Outline each blood parasite and name the species.
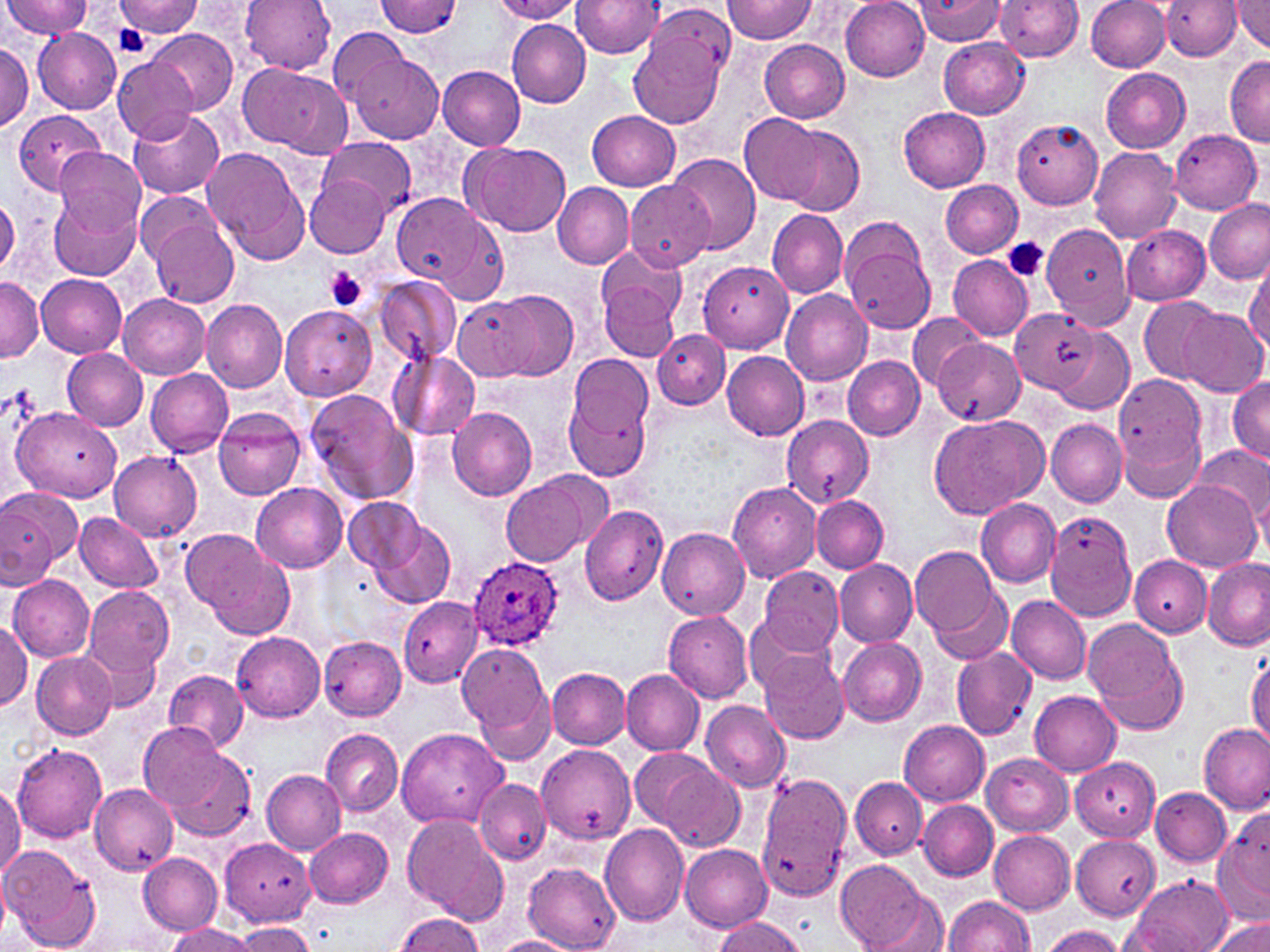

Approximate bounding boxes as (x1,y1)-(x2,y2) corner pairs in pixels.
Plasmodium ovale-infected red blood cells: (469,557)-(563,651).
No Plasmodium falciparum, Plasmodium malariae, Plasmodium vivax, Babesia divergens, or Trypanosoma brucei observed.

slide-level diagnosis = Plasmodium ovale
uninfected red blood cell locations = approximate bounding boxes as (x1,y1)-(x2,y2) corner pairs in pixels: (241,0)-(338,73), (377,0)-(463,37), (720,0)-(816,44), (840,0)-(931,81), (913,0)-(1006,45), (994,0)-(1084,61), (1086,0)-(1170,72), (1162,0)-(1244,61), (1231,0)-(1270,53), (0,1)-(89,40), (113,1)-(203,37), (489,1)-(580,23), (571,1)-(665,59), (637,2)-(734,80), (507,19)-(591,108), (32,26)-(121,114), (327,27)-(414,110), (630,27)-(725,131), (147,29)-(237,115), (939,38)-(1029,118), (759,40)-(849,124), (0,43)-(32,131), (350,52)-(441,143), (113,55)-(196,143), (1224,55)-(1270,146), (238,63)-(347,153), (437,65)-(526,150), (1100,68)-(1191,152), (898,106)-(991,192), (12,110)-(106,194), (128,110)-(225,199), (587,110)-(680,191), (740,114)-(824,205), (1011,119)-(1103,209), (776,123)-(864,215), (1169,127)-(1262,214), (321,136)-(413,214), (463,141)-(571,234), (1089,146)-(1180,244), (55,147)-(146,236), (201,148)-(305,253), (669,152)-(760,254), (305,175)-(390,257), (625,180)-(716,273), (939,180)-(1021,257), (553,183)-(632,269), (136,190)-(225,270), (393,193)-(484,285), (49,195)-(141,280), (0,199)-(19,278), (1203,199)-(1270,284), (767,209)-(847,299), (149,216)-(239,308), (839,217)-(938,335), (435,218)-(508,306), (1041,222)-(1137,327), (1122,225)-(1211,305), (948,255)-(1033,340), (1245,258)-(1270,356), (698,261)-(793,353), (599,267)-(684,364), (36,275)-(126,358), (374,275)-(462,365), (0,279)-(42,363), (493,289)-(577,381), (781,290)-(872,386), (119,295)-(210,379), (1138,296)-(1220,384), (201,297)-(286,392), (456,297)-(537,380), (279,304)-(376,402), (1176,307)-(1265,396), (1010,308)-(1099,394), (907,313)-(985,390), (1052,328)-(1133,414), (653,330)-(731,409), (932,339)-(1026,426), (63,349)-(148,429), (390,350)-(480,443), (721,350)-(809,439), (843,356)-(924,440), (564,361)-(656,482), (146,368)-(234,458), (1112,372)-(1209,478), (1227,377)-(1270,463), (305,388)-(416,504), (11,405)-(122,502), (446,406)-(537,501), (214,409)-(306,501), (783,410)-(879,507), (933,413)-(1048,517), (1047,420)-(1127,508), (1121,425)-(1203,503), (1195,444)-(1270,522), (109,451)-(203,543), (500,476)-(590,567), (1163,479)-(1260,572), (726,481)-(821,584), (1253,481)-(1269,560), (250,483)-(348,573), (0,485)-(82,581), (344,495)-(427,576), (812,495)-(889,572), (976,498)-(1061,587), (579,505)-(668,605), (75,510)-(163,592), (1042,510)-(1140,620), (370,521)-(457,609), (657,528)-(749,620), (188,535)-(295,637), (911,548)-(1000,637), (1129,554)-(1211,638), (1201,558)-(1270,651), (835,559)-(917,647), (758,566)-(845,654), (8,573)-(95,660), (84,587)-(175,677), (933,588)-(1013,663), (1008,594)-(1091,684), (399,596)-(482,687), (663,610)-(754,703), (744,615)-(831,693), (1083,619)-(1187,734), (0,620)-(32,711), (232,632)-(326,720), (837,635)-(926,726), (319,636)-(405,720), (88,637)-(163,714), (459,641)-(553,752), (951,647)-(1037,738), (31,649)-(116,739), (761,651)-(848,743), (1246,655)-(1270,749), (621,668)-(704,754), (547,669)-(631,749), (163,670)-(247,749), (1030,690)-(1121,776), (701,700)-(790,792), (898,719)-(990,805), (138,723)-(233,810), (1198,723)-(1268,813), (395,727)-(508,828), (320,729)-(403,817), (11,744)-(108,842), (538,746)-(633,845), (629,748)-(717,834), (168,752)-(256,842), (981,753)-(1073,835), (1071,757)-(1160,840), (658,764)-(745,850), (263,770)-(345,855), (757,771)-(853,900), (475,777)-(551,864), (850,777)-(925,859), (88,784)-(178,877), (0,785)-(24,879), (1151,787)-(1231,866), (918,800)-(998,880), (403,814)-(508,922), (1216,816)-(1269,914), (598,824)-(689,927), (304,827)-(392,907), (989,831)-(1074,914), (1073,835)-(1161,920), (220,839)-(317,924), (680,844)-(771,931), (0,845)-(100,952), (138,852)-(223,935), (837,859)-(926,949), (524,863)-(620,951), (1,867)-(11,937), (1128,875)-(1232,951), (877,892)-(948,952), (943,895)-(1034,951), (397,912)-(483,952), (1207,915)-(1270,952), (714,916)-(805,952), (234,922)-(315,951), (165,925)-(258,952), (1042,927)-(1127,951), (492,936)-(576,952)
preparation = thin blood film
magnification = 1000x
platelet locations = approximate bounding boxes as (x1,y1)-(x2,y2) corner pairs in pixels: (113,26)-(152,58), (1004,239)-(1048,282), (325,267)-(367,311)
image size = 1270×952 pixels
modality = optical microscopy
stain = May-Grünwald-Giemsa
field of view = one of a larger specimen